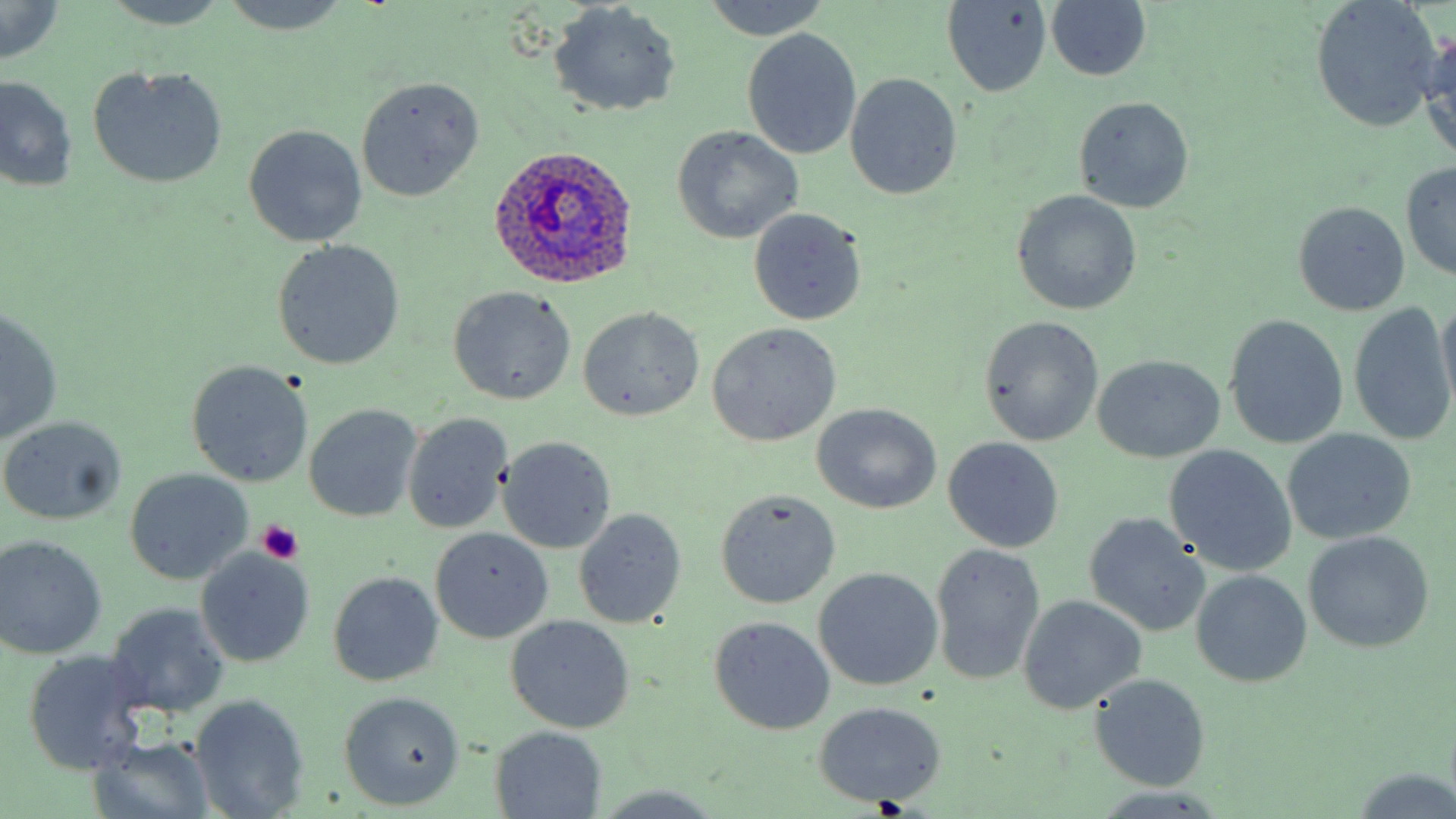
Approximate bounding boxes as (x1,y1)-(x2,y2) corner pairs in pixels. Platelet locations: (256,519)-(303,565). Uninfected red blood cell locations: (219,0)-(349,34), (700,0)-(831,38), (1309,0)-(1444,131), (101,1)-(230,29), (1045,1)-(1152,82), (548,2)-(682,117), (942,2)-(1053,96), (0,3)-(66,63), (1420,27)-(1456,168), (742,29)-(862,159), (86,64)-(228,189), (845,73)-(962,200), (0,77)-(78,194), (356,77)-(484,200), (1073,97)-(1194,214), (242,124)-(369,247), (670,125)-(804,244), (1400,160)-(1456,282), (1010,190)-(1143,316), (1292,201)-(1410,317), (747,208)-(867,326), (273,240)-(405,370), (448,285)-(576,405), (1436,297)-(1455,413), (1348,305)-(1454,443), (578,307)-(705,421), (0,308)-(64,443), (978,315)-(1103,446), (1223,315)-(1349,449), (706,322)-(841,447), (1091,355)-(1226,464), (187,361)-(313,487), (810,402)-(942,513), (305,404)-(422,522), (401,412)-(513,533), (0,416)-(128,527), (1284,429)-(1416,544), (944,435)-(1064,552), (498,437)-(617,553), (1163,444)-(1297,576), (125,470)-(251,583), (714,488)-(841,609), (573,510)-(687,627), (1084,512)-(1210,637), (430,527)-(553,644), (1303,531)-(1436,655), (0,535)-(107,657), (930,543)-(1045,686), (195,550)-(315,667), (813,568)-(942,691), (1191,571)-(1312,688), (328,572)-(444,687), (1017,595)-(1147,715), (107,602)-(230,718), (506,615)-(635,733), (708,615)-(835,735), (24,650)-(145,774), (1090,673)-(1211,790), (339,691)-(465,808), (190,693)-(310,819), (811,701)-(946,806), (490,728)-(607,817), (86,735)-(214,818), (1347,768)-(1456,817), (590,784)-(725,817). Plasmodium ovale-infected red blood cell locations: (483,145)-(641,292). Slide-level diagnosis: Plasmodium ovale. Light microscopy. Single field of view. Image is 1456×819 pixels. Captured at 1000x magnification. Thin blood film. May-Grünwald-Giemsa-stained preparation.